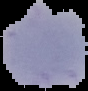

Summary:
  - Image type: cell region segmented out of the field of view; surrounding area masked to black
  - Malaria status: uninfected
  - Preparation: thin blood smear
  - Image size: 88×91 pixels